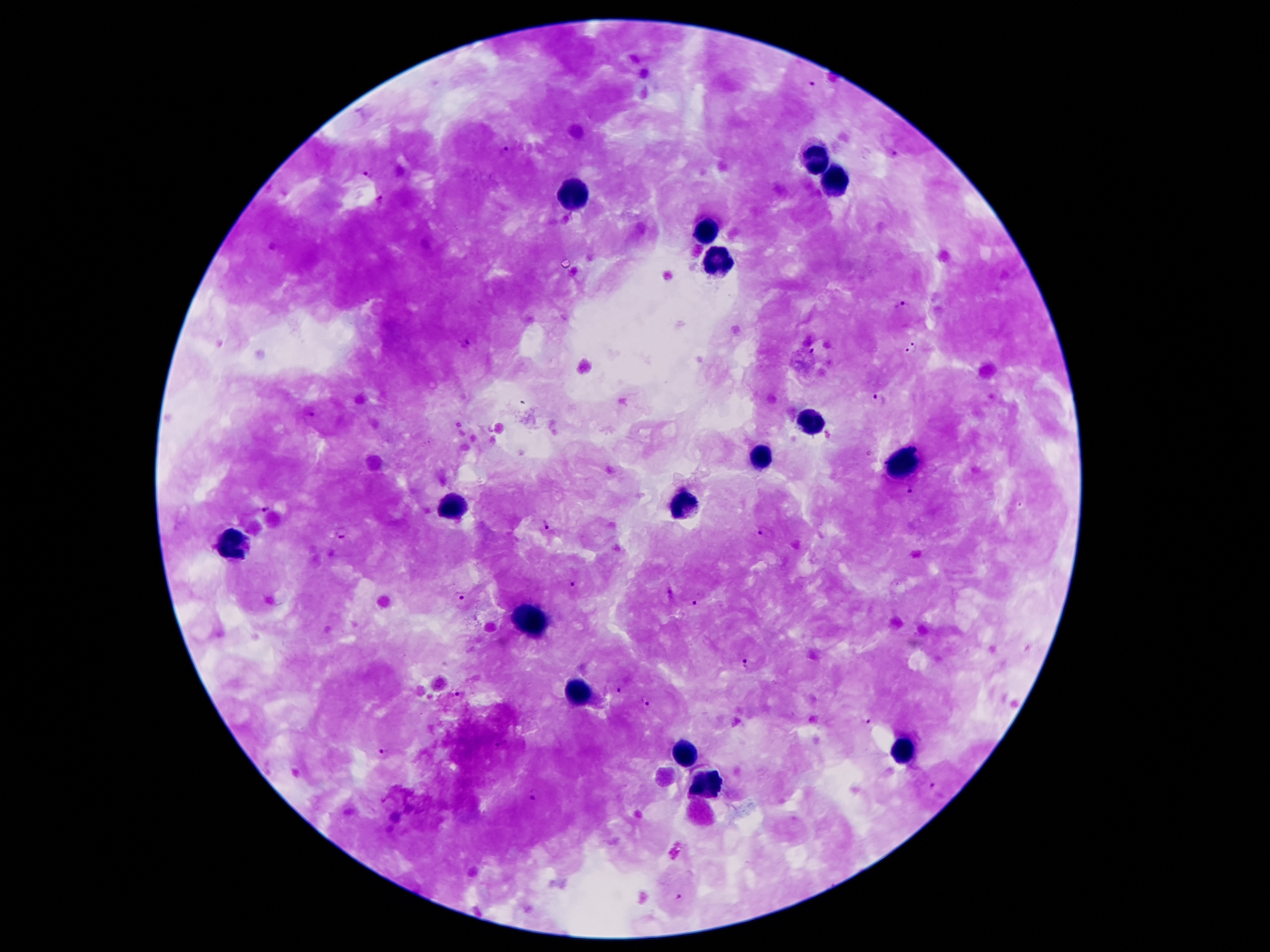

Approximate object centers, in pixels from the top-left corner. Plasmodium parasite locations: (x=810, y=83), (x=504, y=152), (x=894, y=153), (x=369, y=172), (x=381, y=199), (x=905, y=309), (x=466, y=343), (x=912, y=348), (x=813, y=352), (x=879, y=400), (x=309, y=412), (x=911, y=491), (x=266, y=508), (x=545, y=525), (x=764, y=530), (x=342, y=533), (x=571, y=582), (x=465, y=594), (x=695, y=603), (x=747, y=663), (x=619, y=688), (x=459, y=692), (x=646, y=702), (x=866, y=720), (x=501, y=743), (x=384, y=753), (x=931, y=787), (x=534, y=795), (x=679, y=894). Leukocyte locations: (x=818, y=157), (x=834, y=179), (x=575, y=194), (x=707, y=230), (x=718, y=257), (x=809, y=420), (x=763, y=459), (x=900, y=464), (x=679, y=504), (x=450, y=511), (x=230, y=543), (x=534, y=623), (x=577, y=692), (x=686, y=752), (x=902, y=753), (x=707, y=784). Patient malaria status: infected with Plasmodium falciparum. Single field of view. Thick blood smear. Smartphone photograph taken through the microscope eyepiece. 100x magnification. Image is 1270×952 pixels. Giemsa-stained preparation.